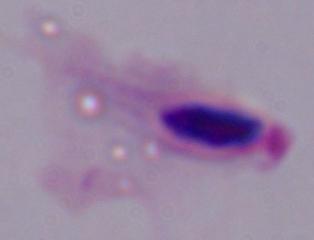

1000x magnification. A trichomonad is shown. Photomicrograph.